Comment on the morphology of the erythrocytes.
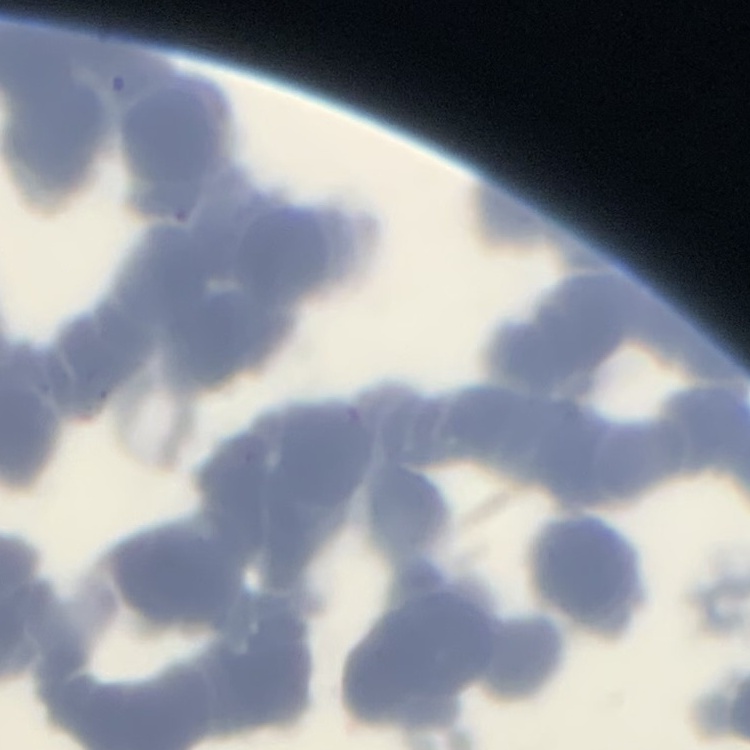
Rouleaux formation.

One tile cut from a larger photomicrograph. Field's or Giemsa stain. Thin blood smear.